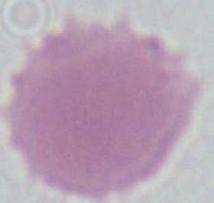
Summary:
  - Identification: red blood cell
  - Modality: photomicrograph
  - Magnification: 1000x